Point out each Plasmodium parasite.
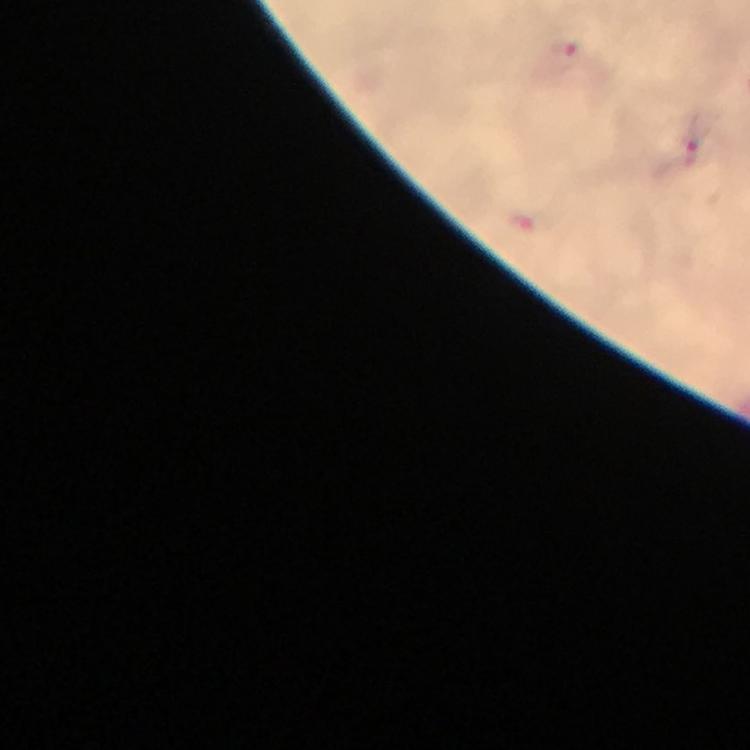
Approximate centers as [x, y] in pixels.
Plasmodium parasites: [572, 53], [523, 225].

stain: Giemsa
context: from a malaria diagnostic workup
capture: smartphone mounted on the microscope
image_size: 750×750 pixels
cropped_from: one field of view
preparation: thick blood smear
magnification: 100x
immersion_oil: applied